Assess this cell for malaria.
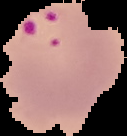
Parasitized.

image size = 127×136 pixels
preparation = thin blood film
image type = segmented cell region on a black background